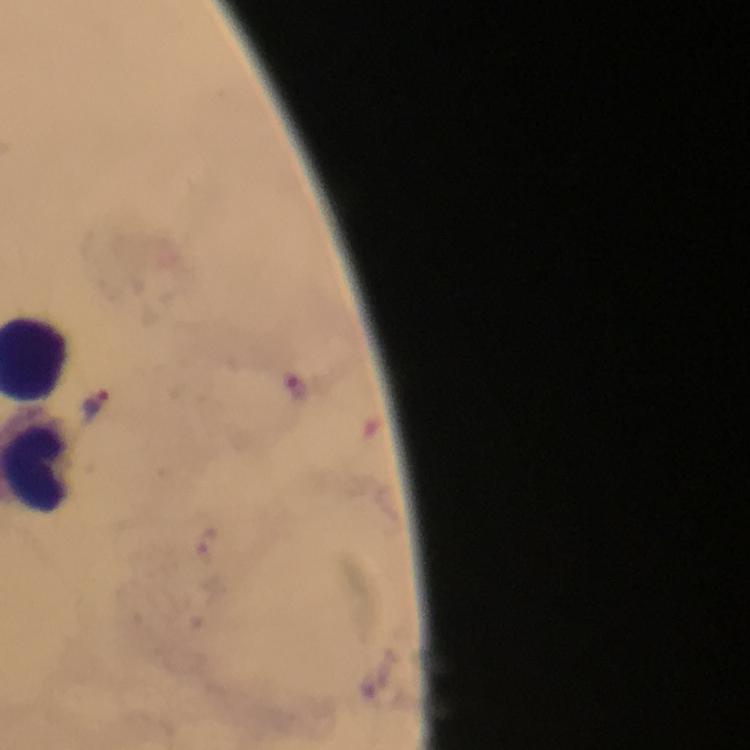
Approximate centers as {x, y} in pixels. Malaria parasite locations: {297, 388}, {97, 400}, {208, 541}. 100x magnification. From a malaria diagnostic workup. Image is 750×750 pixels. A crop from one field of view. Photographed with a smartphone mounted on the microscope. Immersion oil applied. Giemsa-stained preparation. Thick smear.